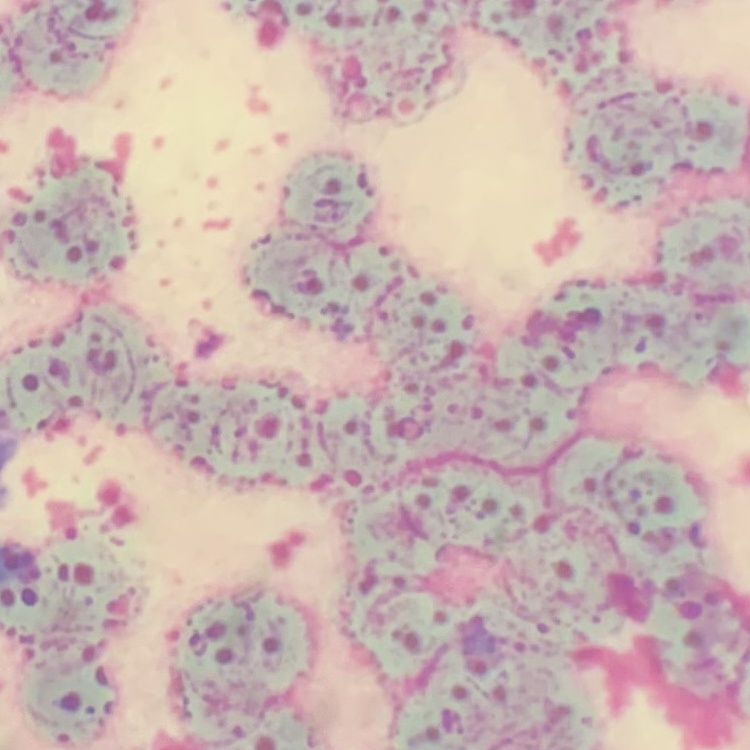
erythrocyte morphology = rouleaux formation
stain = Field's or Giemsa
preparation = thin blood film
image type = one tile cut from a larger photomicrograph